Assess the morphology of the red blood cells.
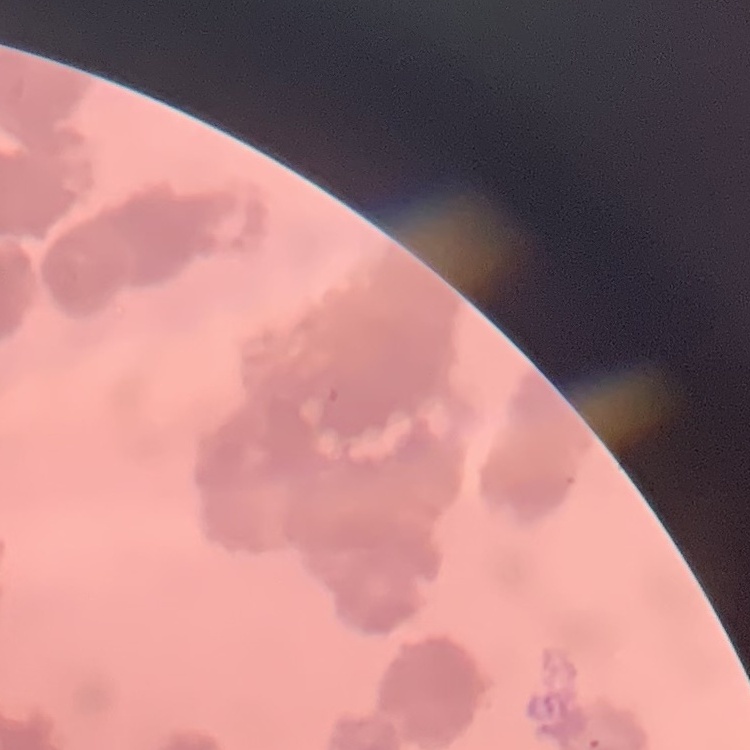

They show rouleaux formation.

Summary:
  - Preparation: thin peripheral smear
  - Image type: one tile cut from a larger photomicrograph
  - Stain: Field's or Giemsa